Describe the morphology of the red blood cells.
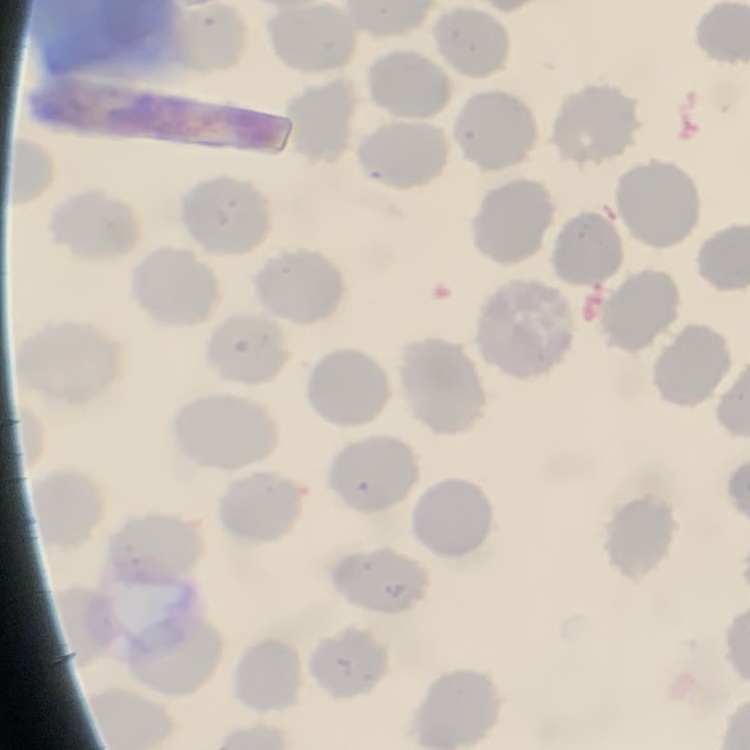
No rouleaux formation.

Summary:
  - Preparation: thin blood smear
  - Stain: Field's or Giemsa
  - Image type: one tile cut from a larger photomicrograph